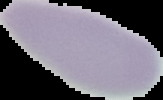
image type = segmented cell region with the area outside set to black
preparation = thin blood film
image size = 163×100 pixels
malaria status = uninfected